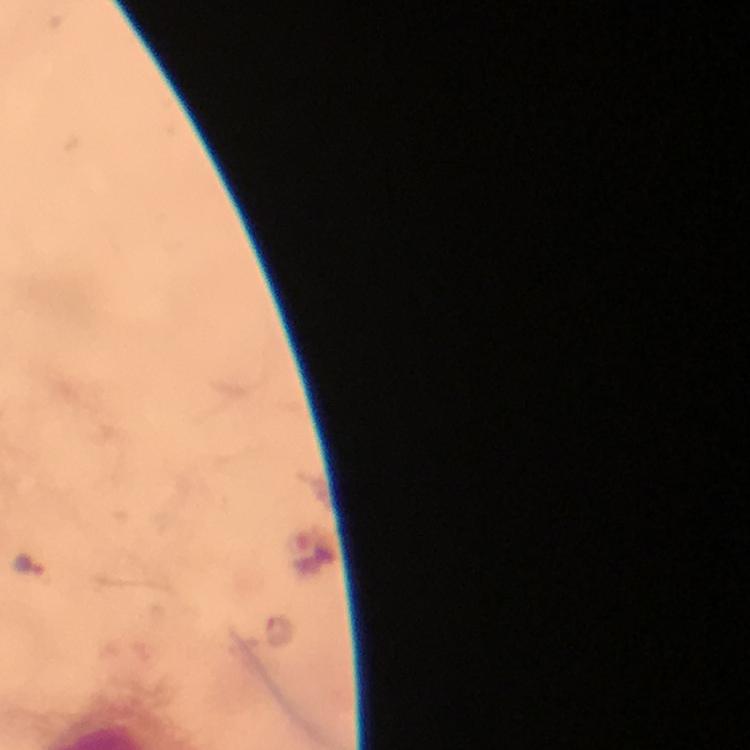

cropped_from: one field of view
capture: smartphone camera through the microscope
context: from a diagnostic examination for malaria
stain: Giemsa
malaria_parasite_locations: 'approximate centers as [x, y] in pixels: [27, 564], [280, 630]'
magnification: 100x
preparation: thick blood film
immersion_oil: used
image_size: 750×750 pixels